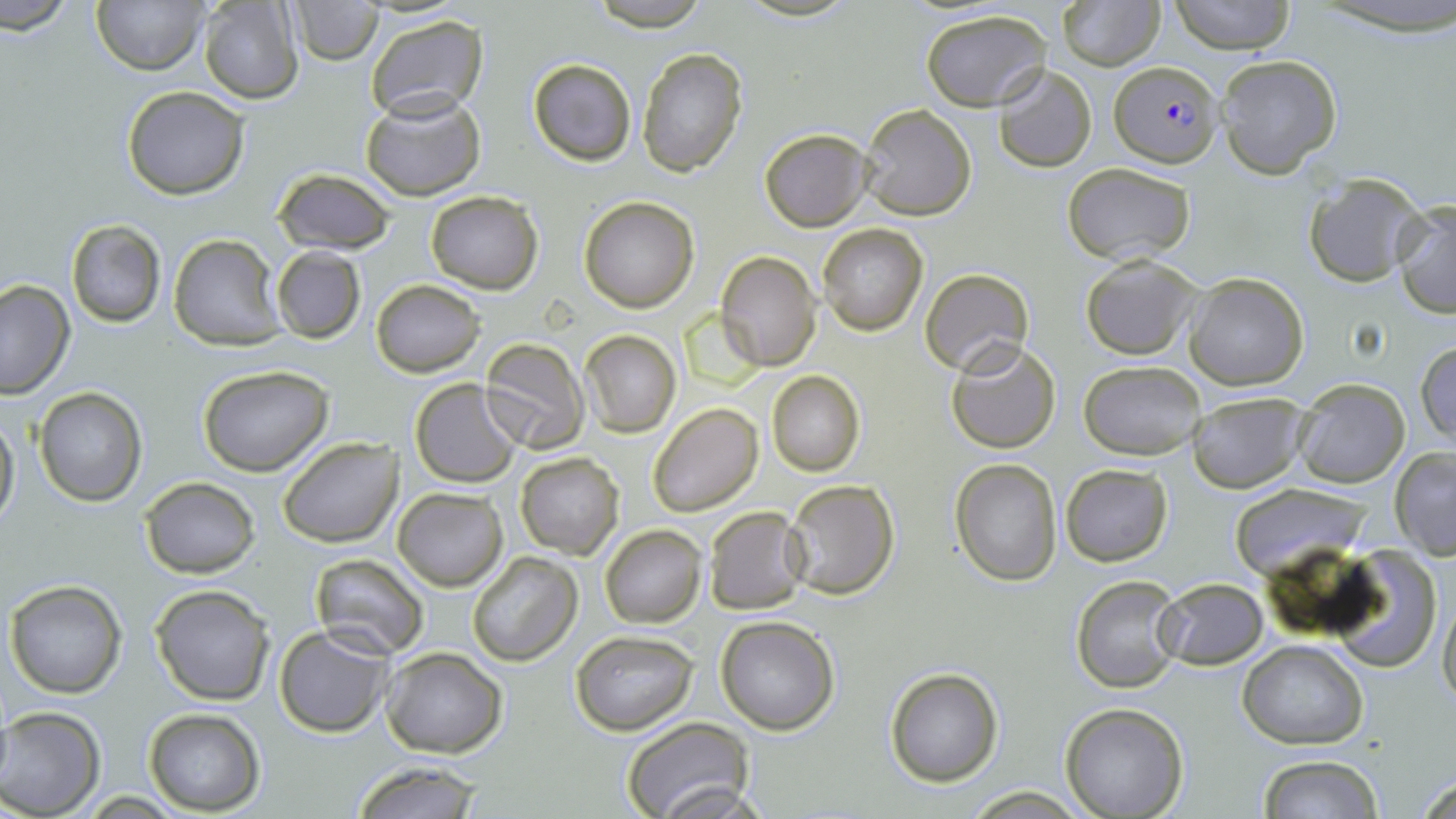

Approximate bounding boxes as [x1, y1, x2, y2] in pixels. Plasmodium falciparum-infected red blood cell locations: [1108, 59, 1222, 167]. Uninfected red blood cell locations: [4, 0, 76, 37], [91, 0, 211, 74], [289, 0, 383, 64], [587, 0, 711, 29], [1056, 0, 1166, 70], [1169, 0, 1294, 53], [198, 1, 304, 104], [919, 8, 1054, 111], [365, 15, 489, 123], [637, 45, 747, 176], [1216, 54, 1342, 177], [528, 58, 636, 167], [993, 65, 1097, 173], [122, 85, 249, 201], [361, 92, 487, 202], [859, 103, 977, 221], [758, 128, 872, 231], [1062, 163, 1195, 264], [272, 168, 396, 256], [1302, 172, 1429, 286], [424, 190, 544, 293], [578, 197, 701, 313], [1391, 197, 1456, 317], [64, 218, 166, 328], [817, 223, 929, 336], [167, 233, 285, 349], [271, 249, 366, 343], [716, 251, 821, 371], [1080, 252, 1203, 360], [920, 269, 1033, 376], [1184, 274, 1308, 390], [0, 280, 74, 400], [371, 280, 485, 376], [578, 329, 681, 438], [481, 337, 590, 454], [1415, 339, 1456, 445], [945, 340, 1063, 455], [1079, 361, 1206, 460], [197, 364, 333, 476], [766, 370, 865, 476], [409, 378, 521, 487], [1293, 378, 1410, 489], [34, 387, 147, 505], [1188, 395, 1308, 493], [648, 402, 764, 517], [0, 407, 19, 528], [277, 436, 403, 548], [1390, 448, 1456, 559], [515, 452, 625, 560], [950, 458, 1062, 586], [1061, 463, 1174, 566], [140, 476, 261, 578], [782, 478, 901, 600], [1228, 482, 1369, 575], [392, 487, 507, 591], [703, 506, 809, 615], [600, 525, 706, 627], [1323, 548, 1446, 673], [467, 551, 583, 667], [310, 552, 431, 660], [1071, 574, 1184, 695], [4, 578, 128, 700], [1153, 578, 1268, 669], [150, 583, 276, 704], [1437, 585, 1456, 711], [714, 615, 840, 735], [273, 625, 395, 736], [570, 630, 698, 735], [1238, 640, 1367, 749], [382, 646, 508, 757], [884, 667, 1002, 787], [1059, 702, 1189, 818], [0, 706, 105, 819], [143, 709, 265, 814], [620, 716, 755, 819], [1257, 755, 1387, 818], [349, 760, 487, 819], [1410, 767, 1456, 819], [960, 788, 1093, 818]. Slide-level diagnosis: Plasmodium falciparum. May-Grünwald-Giemsa-stained preparation. Thin blood smear. Light microscopy. Image is 1456×819 pixels. One field of a larger specimen. 1000x magnification.